Assess for malaria.
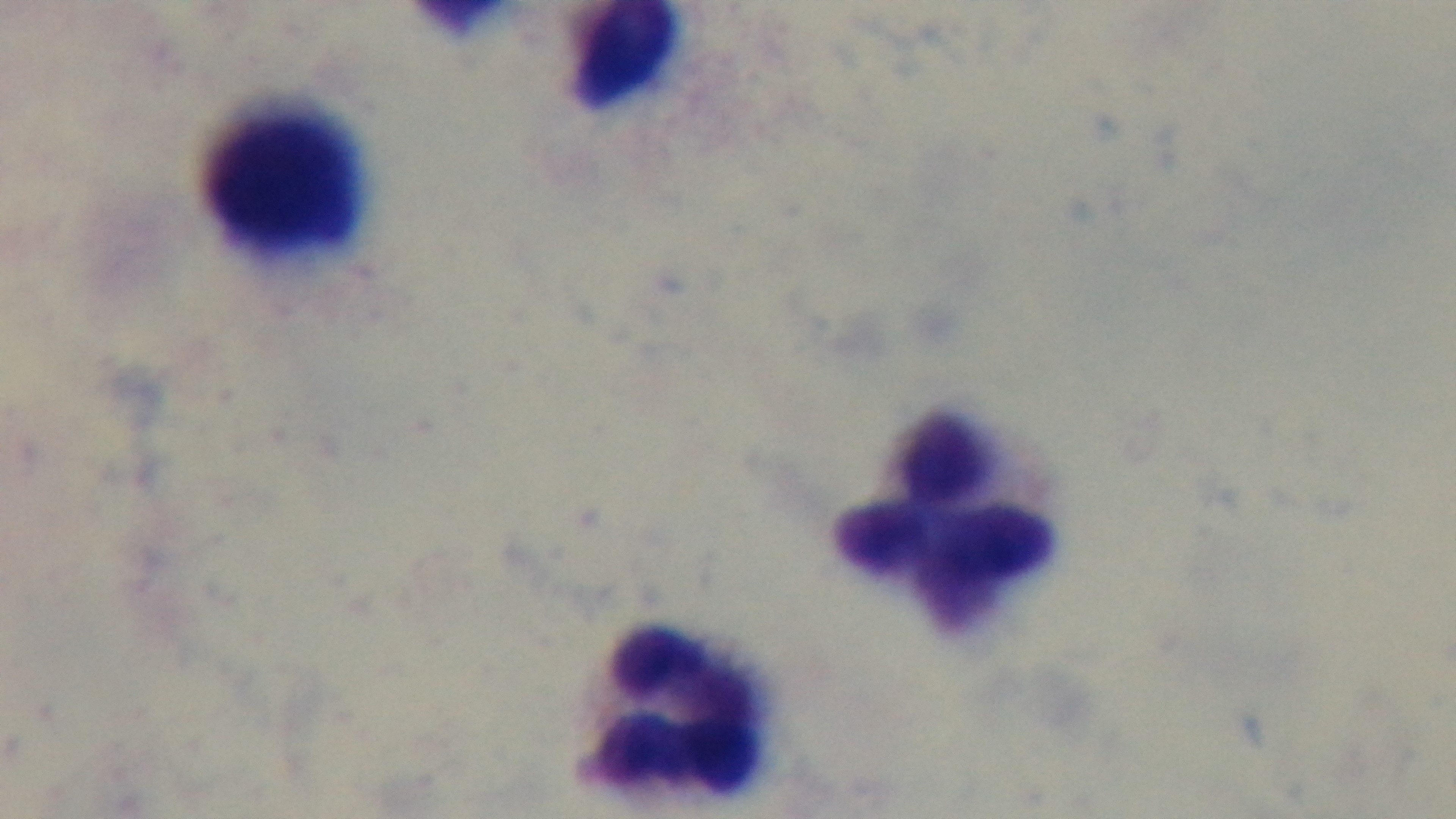
Uninfected.

Summary:
  - Preparation: thick blood film
  - Field of view: one from the slide
  - Capture: mounted 4K digital camera
  - Stain: Giemsa
  - Objective: 100x oil immersion
  - Modality: light microscopy